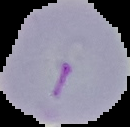
Cell region segmented out of the field of view; the surrounding area is masked to black. Malaria status: parasitized. From a thin blood smear. Image is 130×127 pixels.